Point out each Plasmodium parasite and each leukocyte.
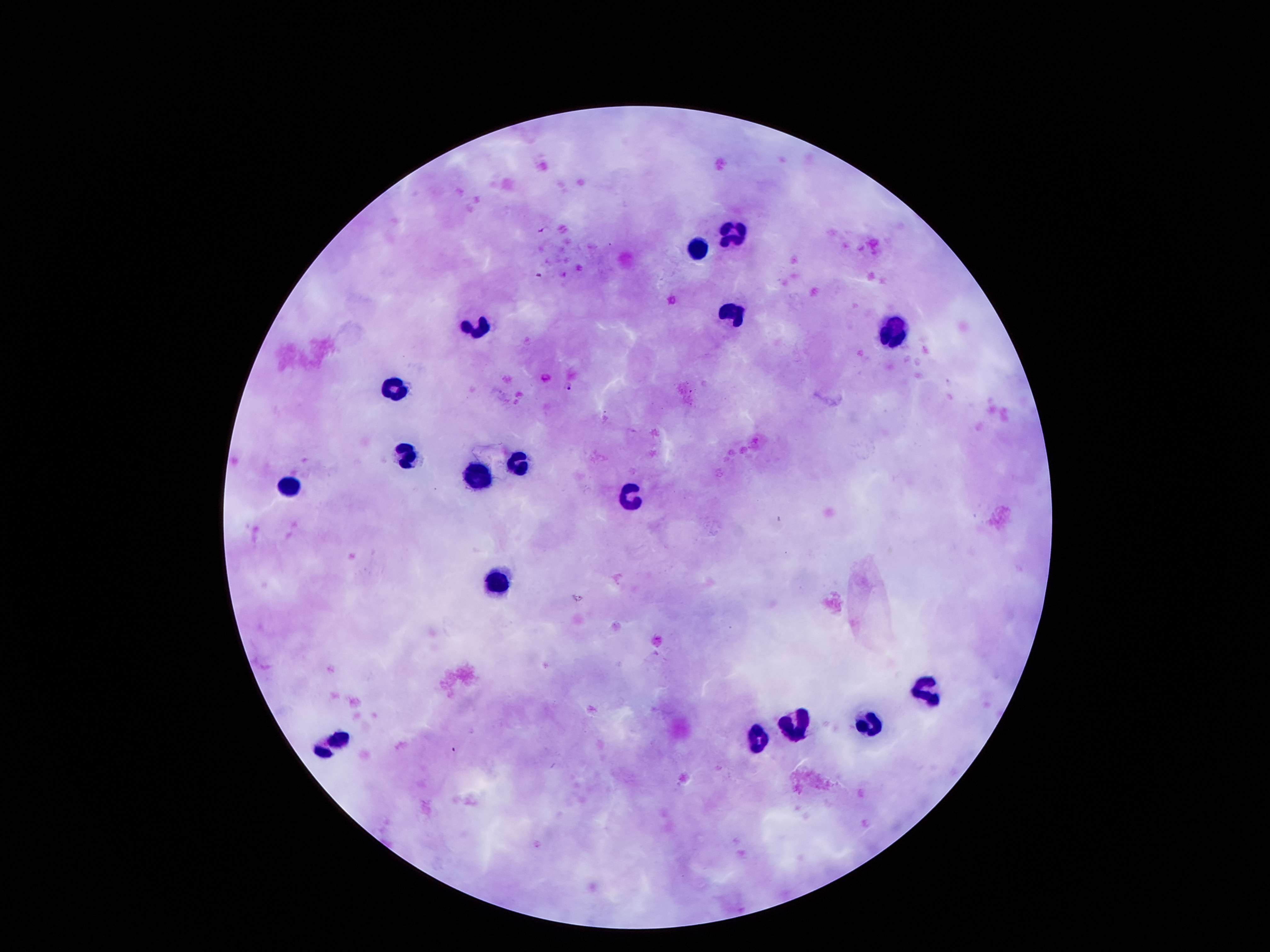

Approximate centers as {x, y} in pixels.
Plasmodium parasites: {540, 275}, {568, 388}, {453, 748}.
Leukocytes: {735, 235}, {697, 248}, {735, 314}, {481, 325}, {892, 333}, {395, 387}, {407, 454}, {519, 463}, {479, 472}, {289, 485}, {630, 499}, {495, 583}, {926, 693}, {796, 719}, {869, 722}, {338, 737}, {758, 739}.

preparation: thick peripheral-blood smear
stain: Giemsa
capture: smartphone through the microscope eyepiece
field_of_view: single
magnification: 100x
image_size: 1270×952 pixels
patient_malaria_status: infected with Plasmodium falciparum